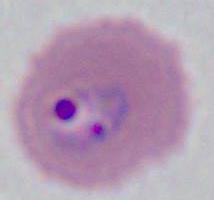
Micrograph. Captured at either 400x or 1000x magnification. A Plasmodium parasite is shown.